State which cell type is depicted.
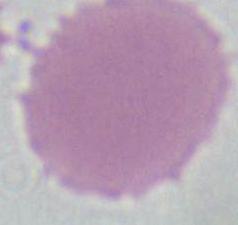
An erythrocyte.

1000x magnification. Photomicrograph.